Report the malaria status of this cell.
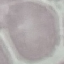
It is uninfected.

Giemsa stain. Photographed with a smartphone camera at the microscope eyepiece. Thin smear of blood. Cell patch, automatically extracted from a larger field of view and resized to 64 × 64 pixels.